Report the malaria status of this cell.
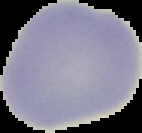

Uninfected.

From a thin blood film. Image is 142×133 pixels. Segmented cell region on a black background.